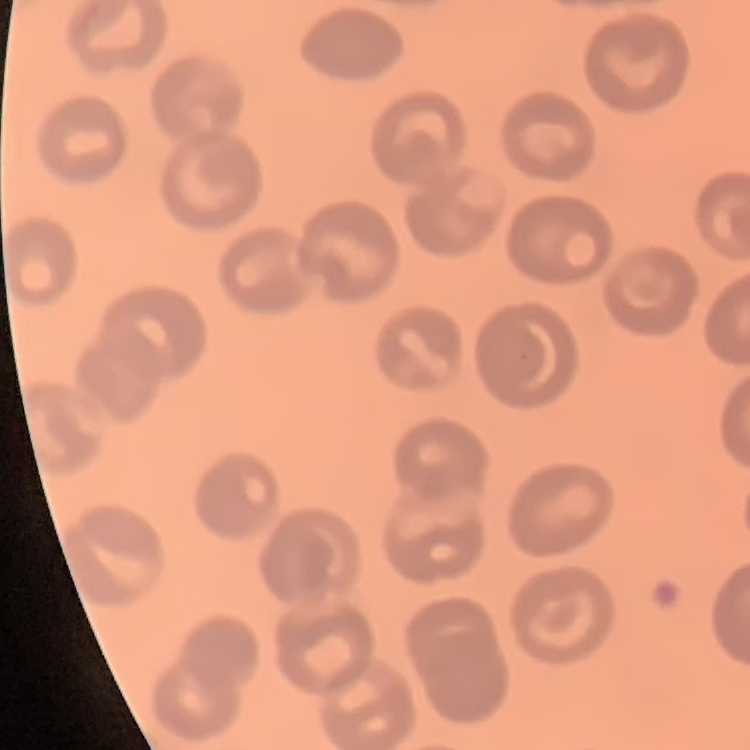
{
  "erythrocyte_morphology": "no rouleaux formation",
  "image_type": "square crop of a larger photomicrograph",
  "stain": "Field's or Giemsa",
  "preparation": "thin peripheral smear"
}